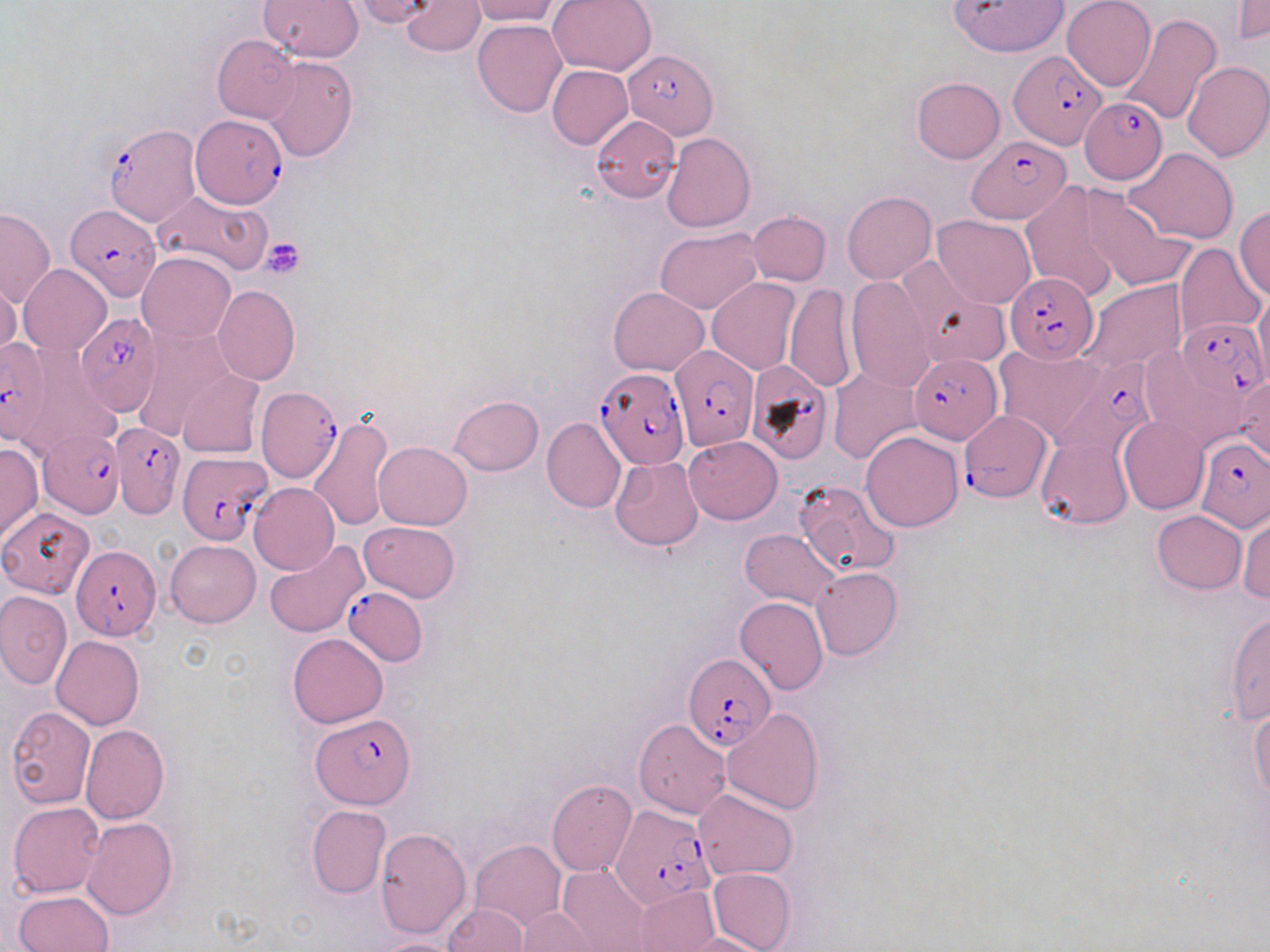

Approximate bounding boxes as named x1/y1/x2/y2 corners in pixels. Platelet locations: (x1=259, y1=237, x2=306, y2=278). Plasmodium falciparum-infected red blood cell locations: (x1=623, y1=49, x2=717, y2=138), (x1=1009, y1=50, x2=1105, y2=148), (x1=1078, y1=97, x2=1166, y2=182), (x1=190, y1=116, x2=284, y2=211), (x1=102, y1=121, x2=201, y2=227), (x1=967, y1=136, x2=1073, y2=224), (x1=60, y1=207, x2=160, y2=308), (x1=1005, y1=271, x2=1099, y2=363), (x1=73, y1=311, x2=164, y2=424), (x1=1167, y1=319, x2=1266, y2=407), (x1=0, y1=338, x2=55, y2=446), (x1=670, y1=346, x2=758, y2=451), (x1=908, y1=353, x2=1002, y2=443), (x1=1053, y1=354, x2=1157, y2=457), (x1=742, y1=360, x2=835, y2=466), (x1=596, y1=368, x2=690, y2=469), (x1=256, y1=383, x2=342, y2=483), (x1=962, y1=411, x2=1049, y2=502), (x1=112, y1=419, x2=182, y2=519), (x1=34, y1=427, x2=123, y2=515), (x1=1197, y1=438, x2=1268, y2=530), (x1=176, y1=451, x2=271, y2=545), (x1=72, y1=544, x2=160, y2=641), (x1=342, y1=585, x2=428, y2=666), (x1=682, y1=654, x2=775, y2=751), (x1=311, y1=713, x2=416, y2=807), (x1=612, y1=804, x2=717, y2=909). Uninfected red blood cell locations: (x1=257, y1=0, x2=364, y2=61), (x1=347, y1=0, x2=436, y2=25), (x1=400, y1=0, x2=484, y2=57), (x1=468, y1=0, x2=561, y2=26), (x1=547, y1=0, x2=657, y2=76), (x1=951, y1=0, x2=1067, y2=56), (x1=1062, y1=0, x2=1156, y2=90), (x1=1232, y1=0, x2=1268, y2=45), (x1=1117, y1=13, x2=1222, y2=126), (x1=472, y1=19, x2=567, y2=117), (x1=210, y1=34, x2=300, y2=124), (x1=263, y1=55, x2=358, y2=160), (x1=1182, y1=60, x2=1269, y2=162), (x1=547, y1=65, x2=633, y2=150), (x1=911, y1=77, x2=1005, y2=164), (x1=591, y1=116, x2=680, y2=203), (x1=661, y1=132, x2=756, y2=232), (x1=1125, y1=147, x2=1239, y2=243), (x1=1020, y1=182, x2=1123, y2=302), (x1=1081, y1=189, x2=1193, y2=291), (x1=152, y1=190, x2=273, y2=276), (x1=842, y1=191, x2=936, y2=283), (x1=1235, y1=205, x2=1270, y2=300), (x1=0, y1=208, x2=56, y2=308), (x1=746, y1=211, x2=831, y2=286), (x1=932, y1=215, x2=1037, y2=309), (x1=654, y1=228, x2=763, y2=313), (x1=1174, y1=243, x2=1266, y2=344), (x1=138, y1=252, x2=235, y2=343), (x1=895, y1=255, x2=991, y2=352), (x1=19, y1=264, x2=111, y2=356), (x1=845, y1=274, x2=936, y2=393), (x1=0, y1=276, x2=21, y2=362), (x1=706, y1=277, x2=802, y2=374), (x1=1080, y1=279, x2=1187, y2=376), (x1=783, y1=283, x2=857, y2=393), (x1=212, y1=284, x2=300, y2=386), (x1=913, y1=285, x2=1009, y2=370), (x1=608, y1=286, x2=708, y2=375), (x1=1253, y1=288, x2=1270, y2=389), (x1=131, y1=324, x2=234, y2=440), (x1=994, y1=344, x2=1111, y2=443), (x1=1139, y1=350, x2=1250, y2=451), (x1=177, y1=369, x2=265, y2=457), (x1=828, y1=370, x2=924, y2=465), (x1=1229, y1=372, x2=1270, y2=466), (x1=448, y1=396, x2=543, y2=476), (x1=313, y1=415, x2=392, y2=528), (x1=1119, y1=416, x2=1208, y2=514), (x1=541, y1=417, x2=625, y2=512), (x1=861, y1=430, x2=964, y2=532), (x1=684, y1=435, x2=782, y2=524), (x1=1036, y1=435, x2=1132, y2=531), (x1=375, y1=441, x2=471, y2=529), (x1=0, y1=443, x2=42, y2=543), (x1=610, y1=457, x2=704, y2=551), (x1=791, y1=480, x2=900, y2=579), (x1=248, y1=483, x2=340, y2=574), (x1=0, y1=506, x2=95, y2=598), (x1=1151, y1=510, x2=1246, y2=594), (x1=1237, y1=512, x2=1269, y2=603), (x1=358, y1=521, x2=459, y2=603), (x1=741, y1=529, x2=840, y2=608), (x1=165, y1=540, x2=260, y2=627), (x1=264, y1=540, x2=369, y2=638), (x1=811, y1=566, x2=901, y2=660), (x1=0, y1=591, x2=72, y2=686), (x1=735, y1=597, x2=828, y2=694), (x1=1224, y1=612, x2=1270, y2=725), (x1=287, y1=633, x2=387, y2=727), (x1=51, y1=634, x2=144, y2=729), (x1=1249, y1=703, x2=1270, y2=803), (x1=5, y1=706, x2=96, y2=809), (x1=720, y1=708, x2=825, y2=814), (x1=634, y1=719, x2=730, y2=817), (x1=80, y1=724, x2=168, y2=825), (x1=546, y1=779, x2=637, y2=878), (x1=693, y1=788, x2=799, y2=880), (x1=9, y1=801, x2=106, y2=897), (x1=306, y1=805, x2=390, y2=899), (x1=83, y1=816, x2=178, y2=920), (x1=374, y1=827, x2=472, y2=940), (x1=471, y1=840, x2=565, y2=929), (x1=557, y1=866, x2=651, y2=951), (x1=707, y1=867, x2=795, y2=951), (x1=633, y1=885, x2=719, y2=952), (x1=12, y1=889, x2=114, y2=951), (x1=442, y1=903, x2=529, y2=951), (x1=512, y1=908, x2=604, y2=952), (x1=673, y1=932, x2=773, y2=952), (x1=371, y1=937, x2=473, y2=952). Slide-level diagnosis: Plasmodium falciparum. May-Grünwald-Giemsa stain. One field of a larger specimen. 1000x magnification. Thin blood smear. Light microscopy. Image is 1270×952 pixels.